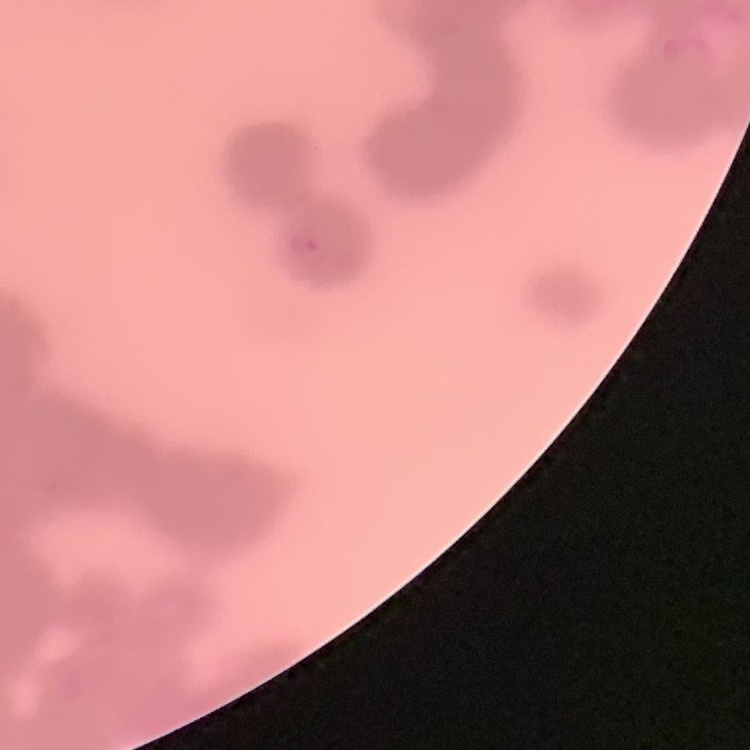 The red blood cells show rouleaux formation. Thin peripheral smear. Field's or Giemsa stain. One tile cut from a larger photomicrograph.